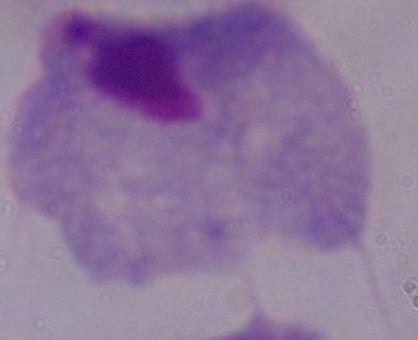
A trichomonad is shown. 1000x magnification. Photomicrograph.